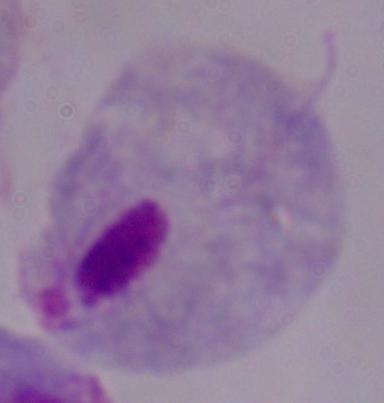

magnification = 1000x
modality = photomicrograph
identification = trichomonad